Assess this cell for malaria.
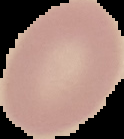

It is uninfected.

Summary:
  - Image size: 124×139 pixels
  - Image type: cell region segmented out of the field of view; surrounding area masked to black
  - Preparation: thin blood film